Assess this cell for malaria.
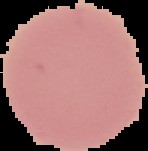
Uninfected.

Summary:
  - Image type: segmented cell region on a black background
  - Preparation: thin blood smear
  - Image size: 148×151 pixels